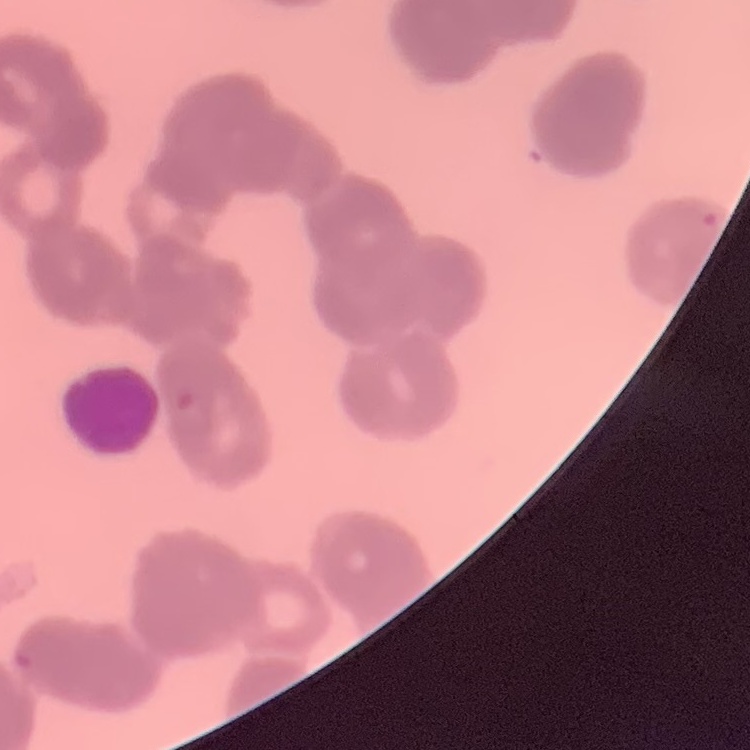 The erythrocytes show rouleaux formation. One tile cut from a larger photomicrograph. Thin blood smear. Field's or Giemsa stain.